State which cell type is depicted.
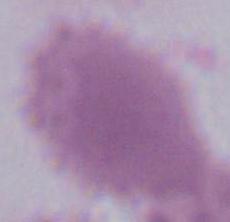
An erythrocyte.

1000x magnification. Photomicrograph.